Assess this cell for malaria.
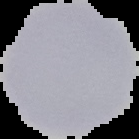

It is uninfected.

Segmented cell region on a black background. From a thin blood film. Image is 139×139 pixels.